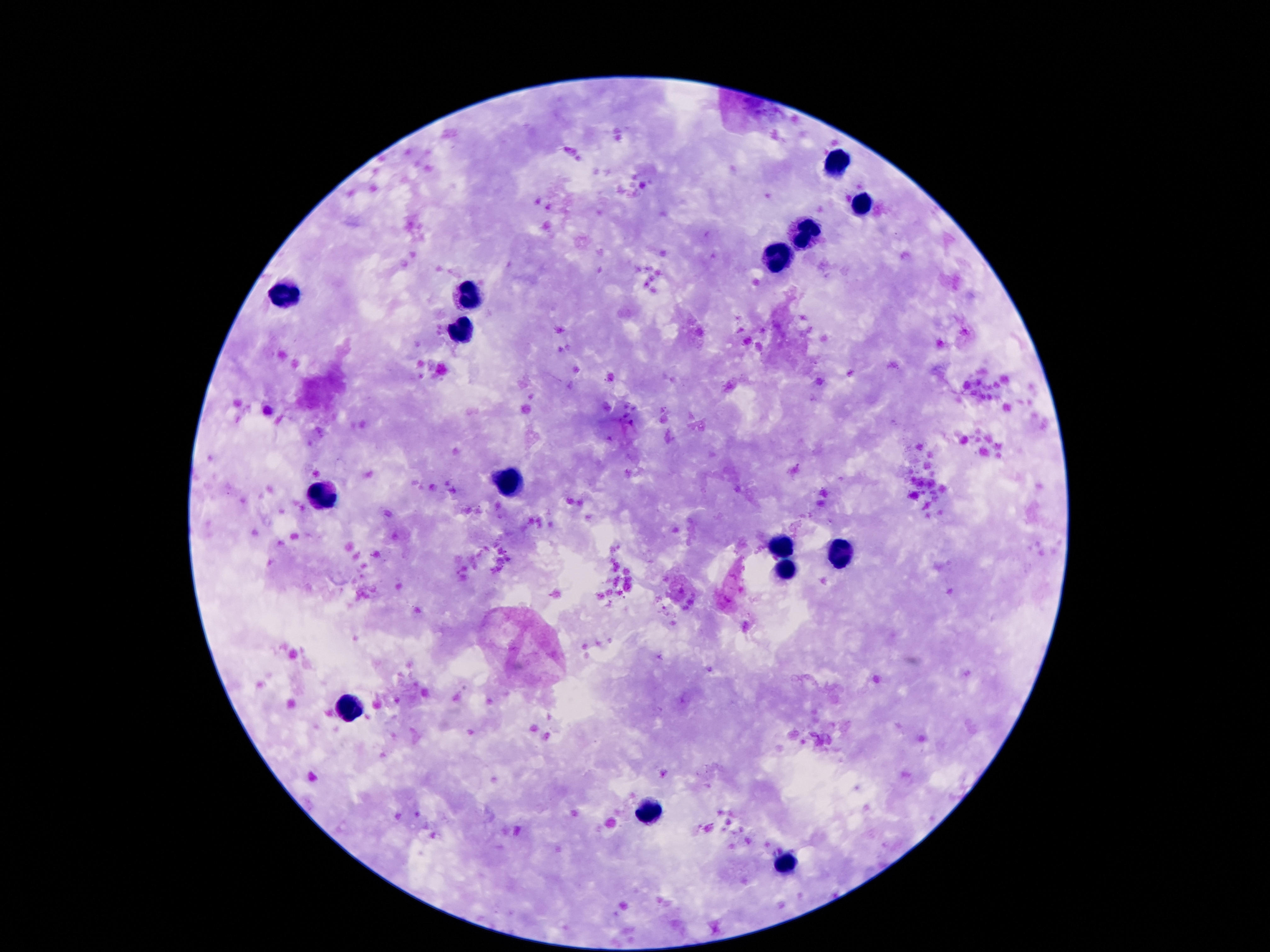
patient malaria status = negative
field of view = single
image size = 1270×952 pixels
stain = Giemsa
preparation = thick peripheral-blood smear
magnification = 100x
capture = smartphone camera through the microscope eyepiece
leukocyte locations = approximate object centers, in pixels from the top-left corner: (x=835, y=162), (x=860, y=205), (x=803, y=235), (x=778, y=258), (x=467, y=292), (x=284, y=297), (x=467, y=327), (x=511, y=481), (x=322, y=495), (x=782, y=547), (x=841, y=552), (x=789, y=565), (x=349, y=708), (x=646, y=813), (x=784, y=864)